Point out each malaria parasite.
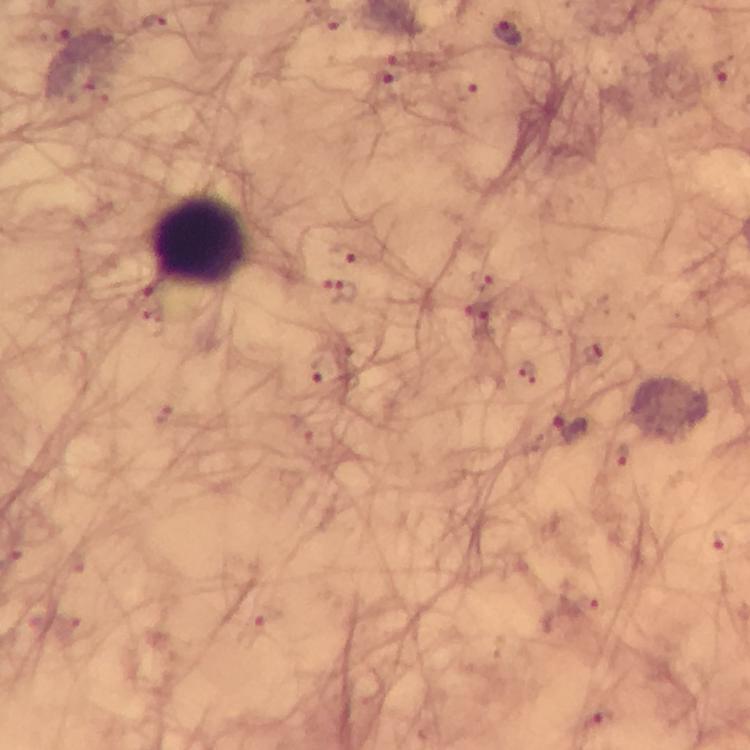
Approximate centers as {x, y} in pixels.
Malaria parasites: {150, 22}, {334, 24}, {55, 28}, {507, 33}, {399, 62}, {723, 70}, {391, 81}, {463, 90}, {342, 254}, {343, 294}, {319, 373}, {569, 427}, {723, 543}, {598, 718}.

cropped_from: one field of view
immersion_oil: used
context: from a diagnostic examination for malaria
magnification: 100x
image_size: 750×750 pixels
preparation: thick blood smear
stain: Giemsa
leukocyte_locations: 'approximate centers as {x, y} in pixels: {200, 243}'
capture: smartphone camera through the microscope